State which cell type is depicted.
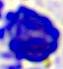

A leukocyte.

magnification = 400x
modality = micrograph